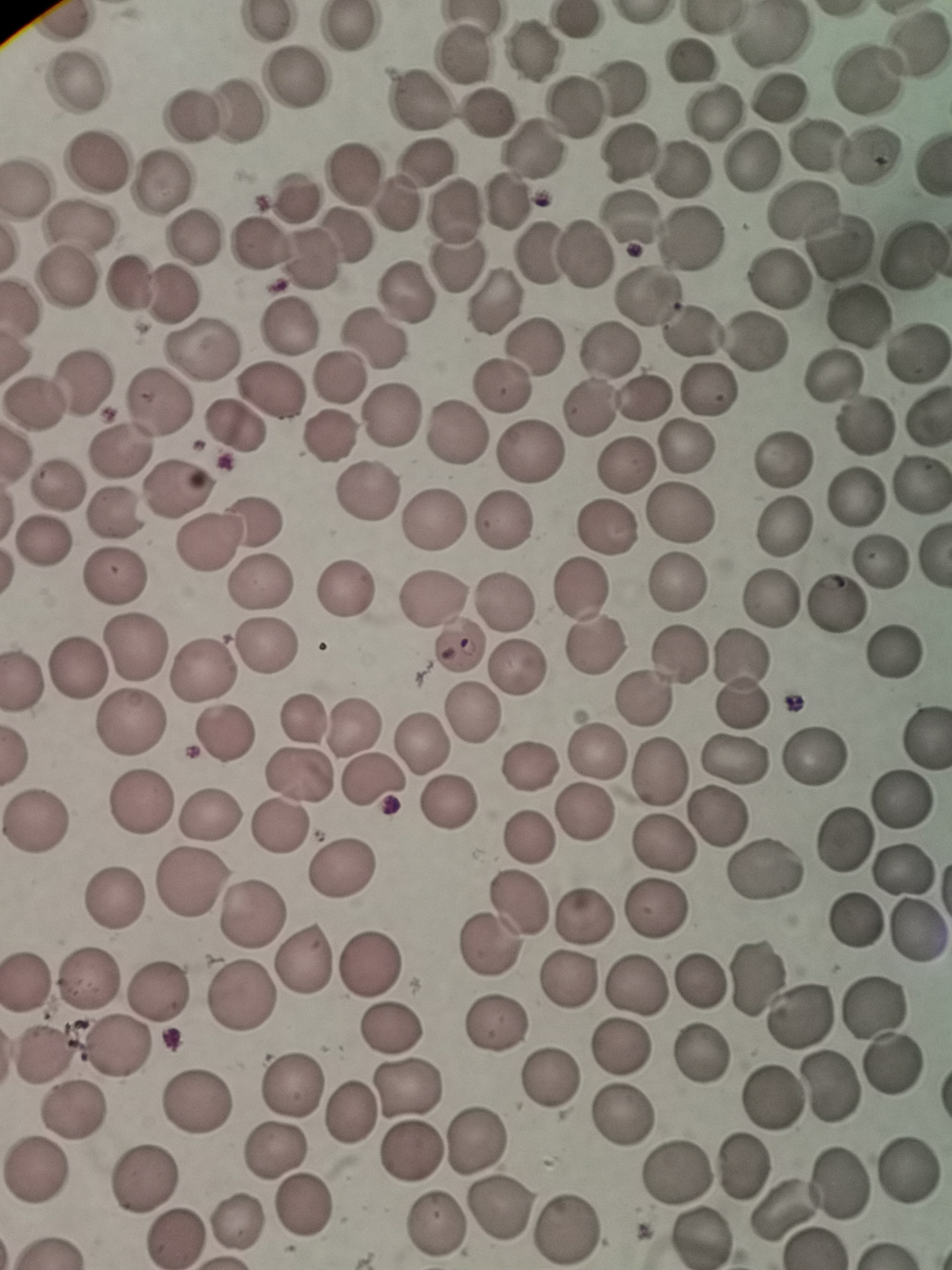
Approximate centers as [x, y] in pixels. Cell locations: [346, 25], [534, 50], [462, 55], [692, 62], [295, 78], [78, 79], [625, 84], [778, 96], [422, 98], [575, 103], [721, 107], [238, 109], [190, 114], [485, 116], [815, 143], [534, 149], [632, 151], [875, 152], [749, 161], [424, 163], [95, 164], [353, 172], [683, 174], [162, 185], [25, 191], [507, 200], [293, 202], [394, 204], [799, 209], [448, 210], [632, 222], [83, 230], [347, 234], [195, 240], [696, 240], [844, 243], [262, 245], [908, 251], [537, 254], [583, 255], [309, 259], [456, 262], [69, 280], [781, 280], [124, 287], [405, 289], [648, 293], [172, 294], [495, 296], [851, 315], [289, 326], [696, 333], [375, 339], [533, 344], [755, 344], [200, 348], [609, 351], [915, 353], [830, 373], [87, 378], [339, 378], [503, 385], [267, 390], [705, 393], [646, 394], [161, 401], [36, 406], [589, 407], [927, 415], [391, 419], [861, 427], [234, 428], [456, 429], [329, 436], [686, 448], [122, 450], [531, 453], [785, 457], [628, 465], [920, 485], [54, 488], [177, 488], [368, 492], [853, 497], [116, 513], [675, 514], [261, 517], [436, 519], [504, 519], [783, 525], [604, 526], [40, 540], [207, 544], [883, 556], [116, 573], [264, 581], [678, 582], [346, 587], [580, 591], [435, 596], [769, 599], [506, 604], [837, 604], [599, 644], [137, 645], [269, 646], [458, 646], [894, 650], [678, 659], [739, 659], [75, 669], [204, 669], [518, 671], [643, 698], [739, 703], [475, 715], [302, 716], [131, 721], [351, 728], [224, 735], [594, 741], [421, 745], [812, 752], [736, 758], [528, 767], [660, 771], [299, 775], [371, 778], [901, 799], [141, 802], [446, 804], [584, 810], [717, 816], [207, 819], [34, 822], [280, 827], [529, 838], [840, 839], [662, 847], [344, 868], [908, 869], [764, 871], [188, 886], [112, 900], [518, 905], [657, 908], [584, 912], [252, 914], [854, 923], [921, 928], [491, 946], [303, 959], [372, 967], [760, 974], [87, 978], [698, 978], [23, 980], [568, 982], [636, 988], [160, 992], [236, 1003], [876, 1006], [802, 1008], [494, 1022], [392, 1026], [622, 1048], [121, 1050], [45, 1053], [697, 1057], [893, 1062], [552, 1079], [290, 1080], [410, 1086], [829, 1086], [771, 1099], [194, 1103], [72, 1112], [348, 1116], [618, 1121], [479, 1135], [277, 1148], [411, 1151], [910, 1168], [741, 1169], [34, 1172], [679, 1173], [147, 1176], [838, 1181], [303, 1209], [499, 1210], [785, 1212], [439, 1220], [234, 1225], [566, 1230], [700, 1235], [175, 1237]. Photographed with a smartphone camera at the microscope eyepiece. Single field of view. Thin smear of blood. Giemsa-stained preparation. Image is 952×1270 pixels.